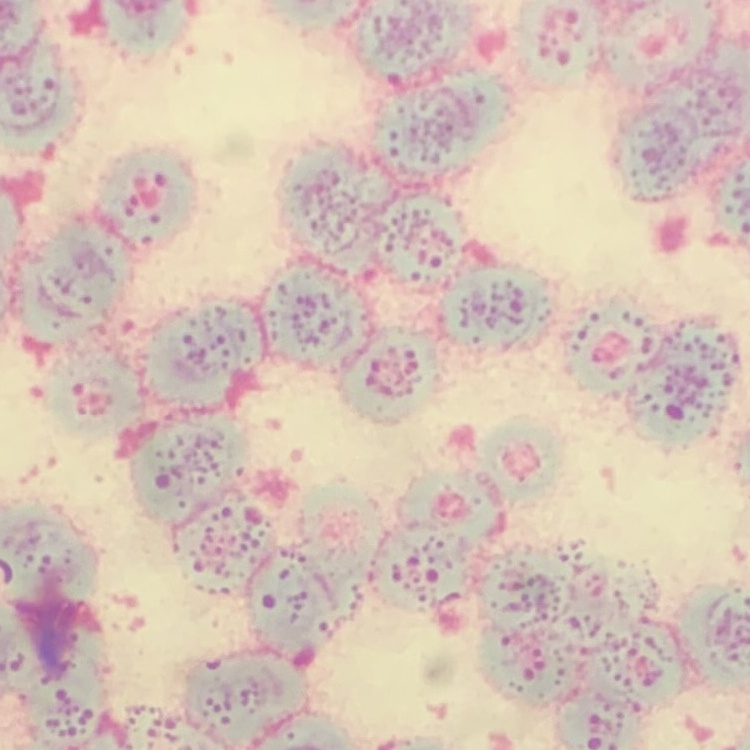
erythrocyte morphology = rouleaux formation
preparation = thin peripheral smear
stain = Field's or Giemsa
image type = square crop of a larger photomicrograph